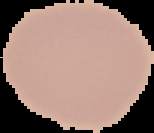
image size = 154×133 pixels
image type = segmented cell region with the area outside set to black
preparation = thin blood film
result = no Plasmodium parasites seen